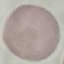
malaria_status: uninfected
image_type: automatically extracted cell patch, resized to 64 × 64 pixels
capture: smartphone through the microscope eyepiece
stain: Giemsa
preparation: thin blood smear